Outline each Babesia divergens-infected red blood cell.
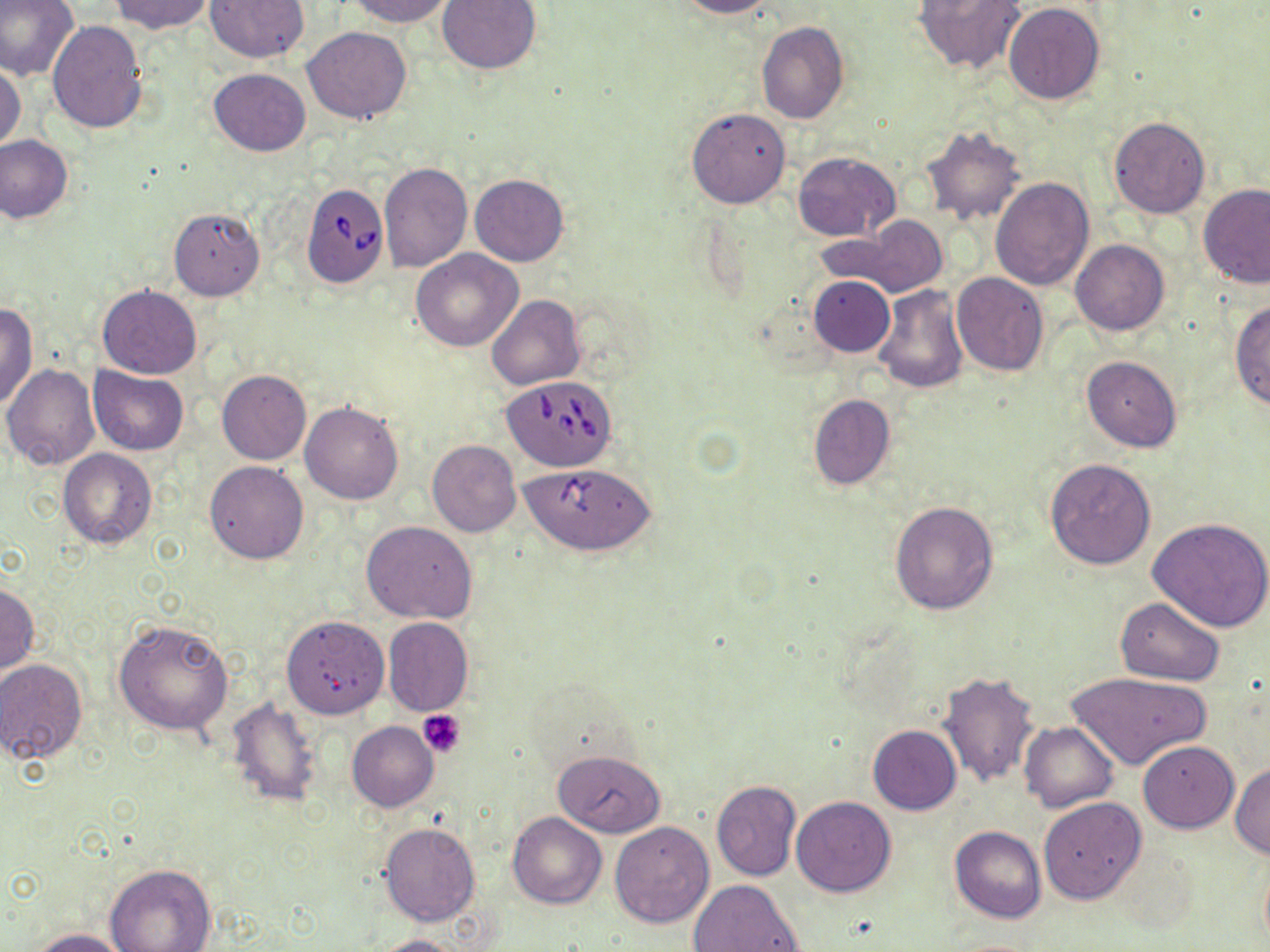

Approximate bounding boxes as (x1,y1)-(x2,y2) corner pairs in pixels.
Babesia divergens-infected red blood cells: (300,182)-(388,288), (500,377)-(615,472), (518,462)-(656,555).

Summary:
  - Platelet locations: (419,712)-(466,758)
  - Uninfected red blood cell locations: (0,0)-(80,82), (110,0)-(214,34), (205,0)-(308,62), (345,0)-(455,26), (437,0)-(542,74), (675,0)-(775,19), (914,0)-(1026,74), (1004,2)-(1105,105), (47,20)-(148,134), (756,22)-(849,123), (302,27)-(413,123), (0,63)-(25,152), (208,69)-(310,156), (687,108)-(792,208), (1107,117)-(1211,219), (920,125)-(1028,226), (1,136)-(73,223), (792,151)-(901,240), (379,163)-(472,272), (470,173)-(569,266), (990,177)-(1095,289), (1199,183)-(1270,287), (168,208)-(265,300), (821,221)-(950,298), (1071,239)-(1169,336), (411,249)-(523,351), (951,273)-(1050,375), (809,275)-(894,357), (97,284)-(202,378), (872,284)-(969,394), (487,294)-(584,390), (0,301)-(37,410), (1231,302)-(1269,411), (1081,356)-(1183,452), (2,363)-(101,471), (89,367)-(188,454), (217,370)-(311,465), (808,394)-(896,490), (300,402)-(405,504), (427,440)-(521,537), (58,449)-(156,551), (1044,457)-(1156,569), (205,460)-(308,563), (890,501)-(999,615), (1148,515)-(1270,634), (361,521)-(478,625), (1,580)-(40,675), (1115,597)-(1225,685), (281,615)-(389,718), (383,617)-(474,715), (114,618)-(234,736), (1,657)-(88,766), (1066,670)-(1211,772), (938,671)-(1041,788), (225,696)-(324,806), (347,721)-(439,811), (1020,721)-(1117,812), (868,725)-(961,814), (1138,741)-(1238,833), (554,750)-(666,837), (1230,761)-(1270,860), (711,780)-(801,881), (791,796)-(897,897), (1039,797)-(1145,905), (507,811)-(607,908), (379,822)-(480,927), (609,822)-(714,927), (950,826)-(1046,924), (105,865)-(215,952), (687,879)-(805,952), (29,929)-(135,951), (370,934)-(473,952)
  - Slide-level diagnosis: Babesia divergens
  - Stain: May-Grünwald-Giemsa
  - Image size: 1270×952 pixels
  - Field of view: one of a larger specimen
  - Magnification: 1000x
  - Preparation: thin blood film
  - Modality: optical microscopy